Name the cell type shown.
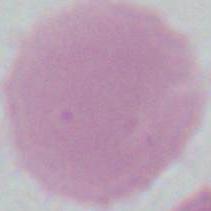

An erythrocyte.

1000x magnification. Micrograph.